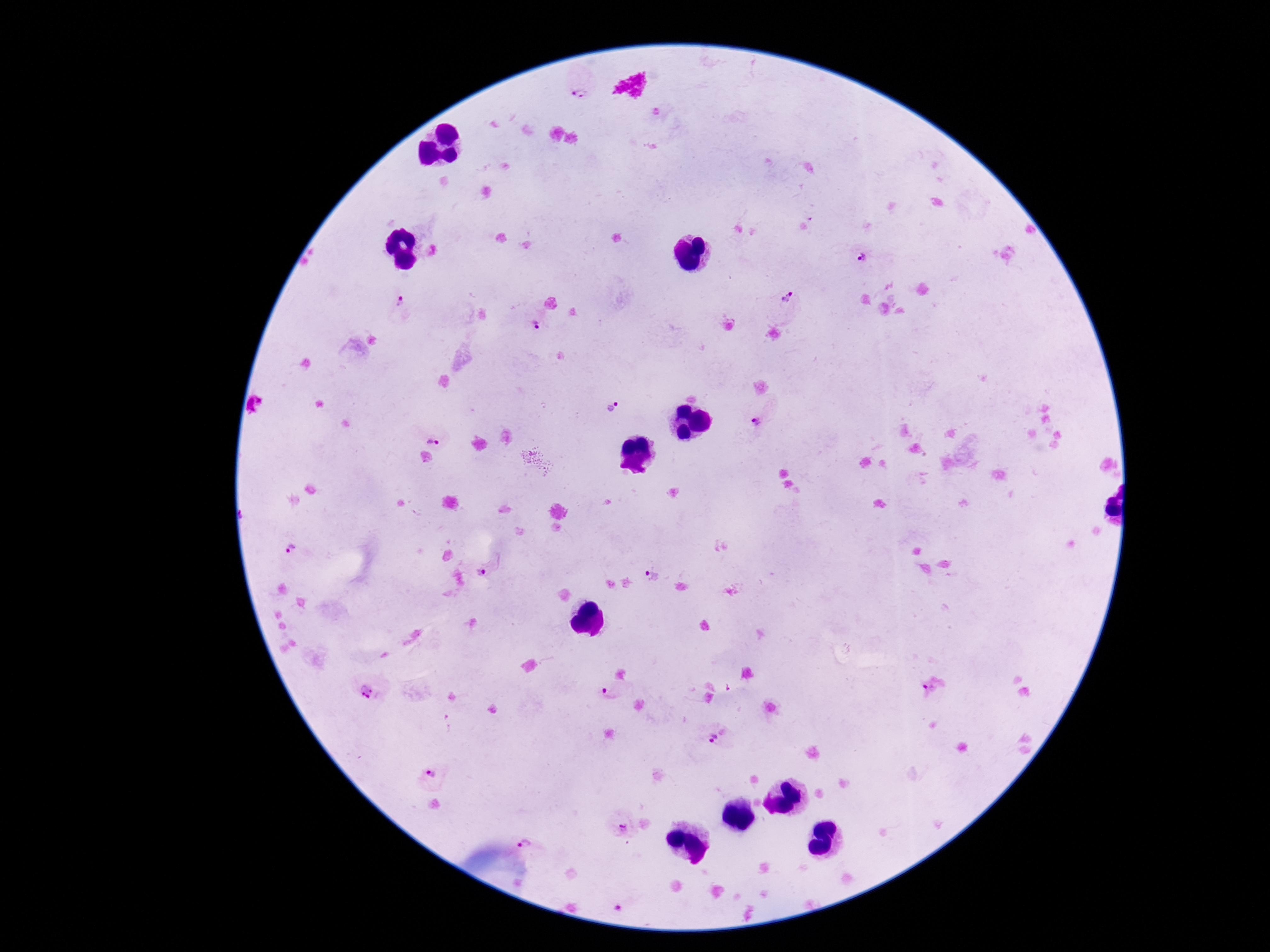

Approximate centers as {x, y} in pixels.
Summary:
  - Plasmodium parasite locations: {581, 94}, {863, 260}, {400, 299}, {788, 302}, {533, 326}, {612, 403}, {758, 424}, {431, 433}, {292, 550}, {484, 570}, {651, 576}, {367, 689}, {928, 692}, {609, 693}, {718, 737}, {432, 777}, {623, 828}, {531, 838}
  - Image size: 1270×952 pixels
  - Magnification: 100x
  - Capture: smartphone camera through the microscope eyepiece
  - Field of view: single
  - Stain: Giemsa
  - Preparation: thick blood smear
  - Patient malaria status: positive